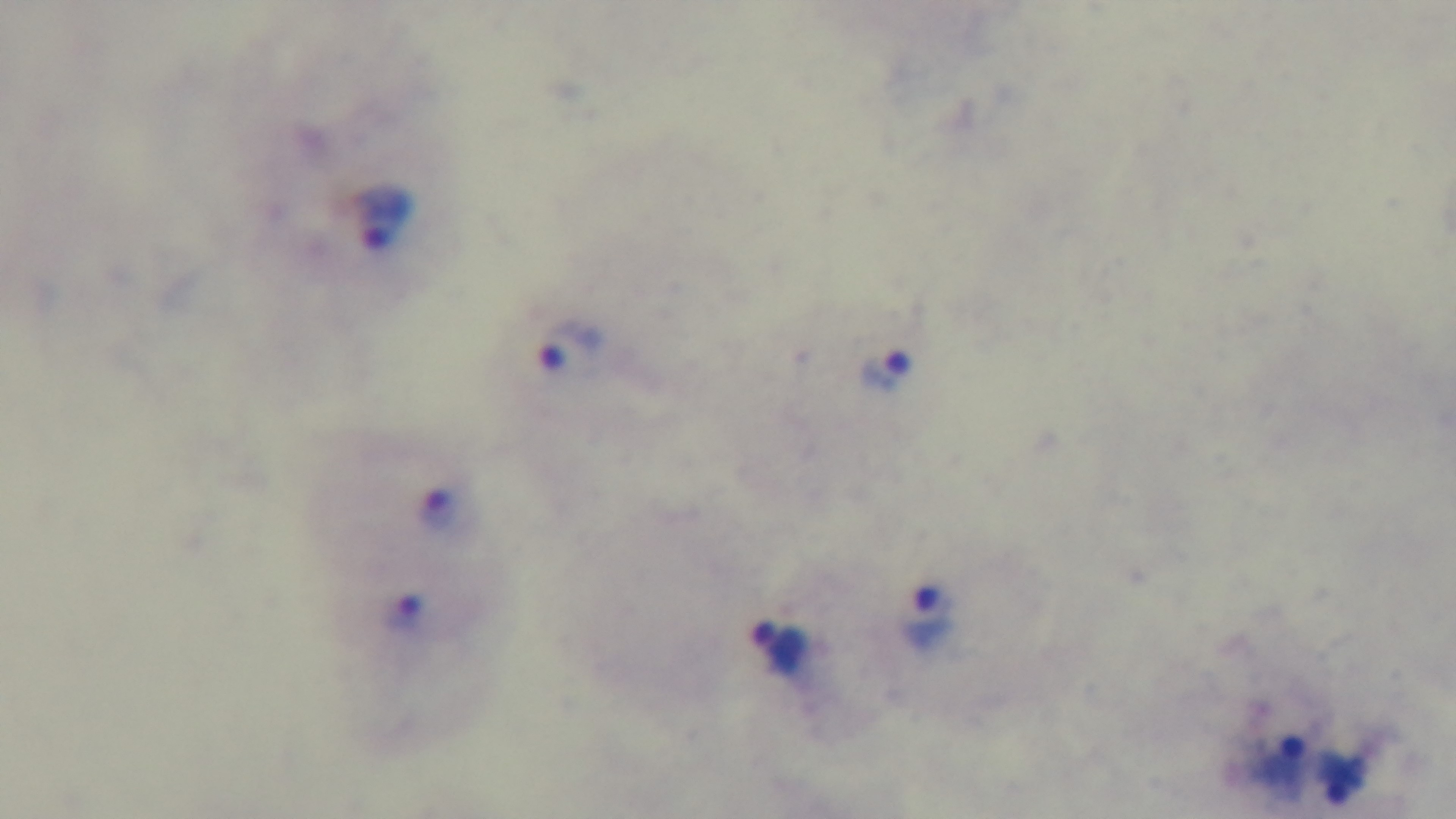

modality = light microscopy
malaria status = infected
field of view = single
preparation = thick smear
capture = mounted 4K digital camera
stain = Giemsa
objective = 100x oil immersion